State the blood parasite species.
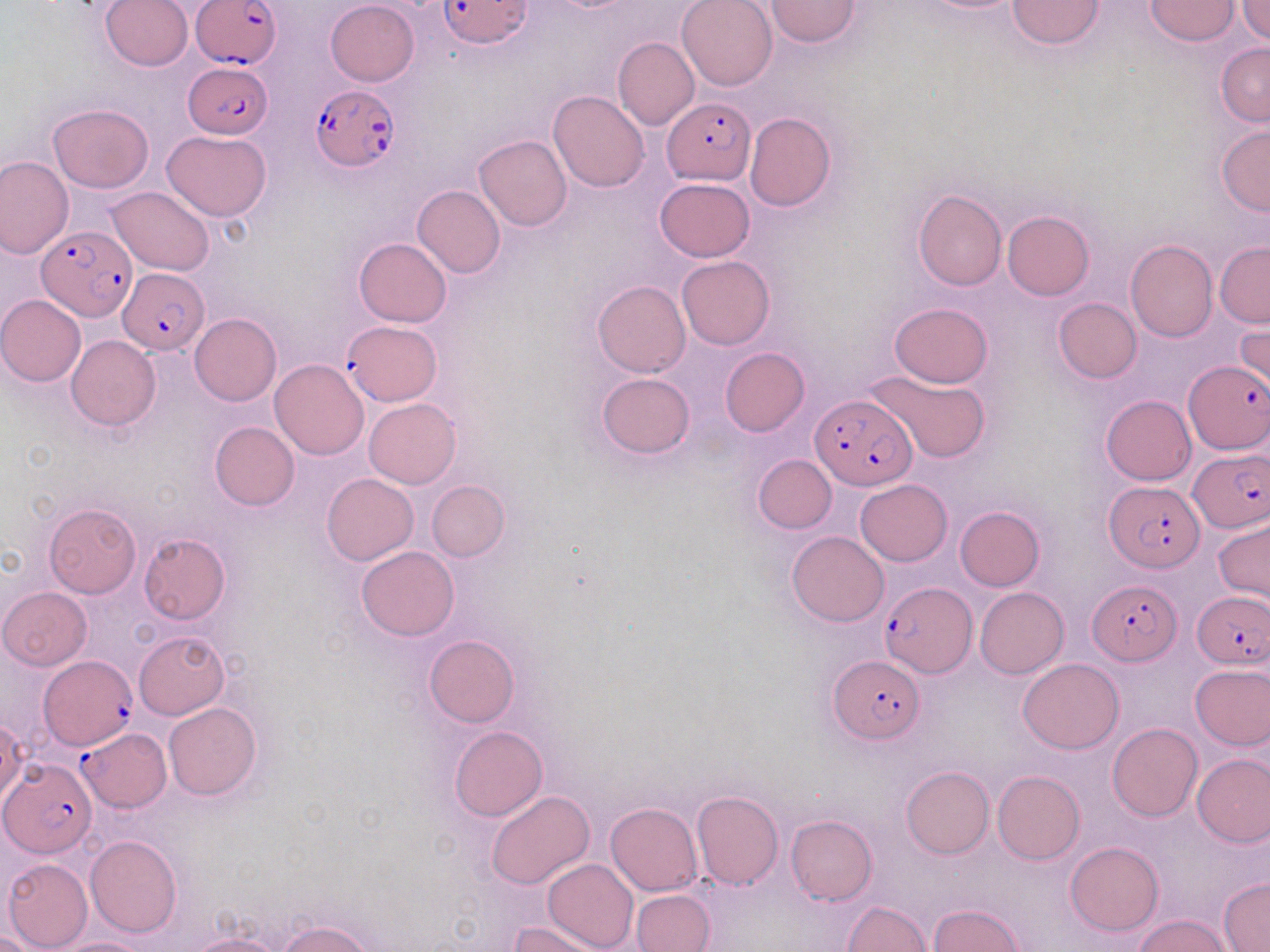
Plasmodium falciparum.

Approximate bounding boxes as named x1/y1/x2/y2 corners in pixels. Plasmodium falciparum-infected red blood cell locations: (x1=190, y1=0, x2=282, y2=68), (x1=437, y1=0, x2=533, y2=49), (x1=187, y1=63, x2=271, y2=140), (x1=310, y1=85, x2=398, y2=172), (x1=662, y1=96, x2=754, y2=183), (x1=36, y1=224, x2=135, y2=323), (x1=118, y1=268, x2=211, y2=355), (x1=342, y1=321, x2=442, y2=405), (x1=1185, y1=360, x2=1270, y2=453), (x1=811, y1=393, x2=915, y2=490), (x1=1190, y1=450, x2=1269, y2=531), (x1=1104, y1=480, x2=1204, y2=571), (x1=1087, y1=580, x2=1180, y2=664), (x1=879, y1=581, x2=974, y2=676), (x1=1193, y1=591, x2=1270, y2=669), (x1=827, y1=654, x2=923, y2=743), (x1=36, y1=655, x2=136, y2=753), (x1=77, y1=727, x2=172, y2=811), (x1=1, y1=759, x2=96, y2=857). Uninfected red blood cell locations: (x1=102, y1=0, x2=192, y2=72), (x1=676, y1=0, x2=777, y2=90), (x1=766, y1=0, x2=861, y2=46), (x1=1008, y1=0, x2=1105, y2=49), (x1=1146, y1=0, x2=1239, y2=44), (x1=1236, y1=0, x2=1270, y2=44), (x1=325, y1=1, x2=419, y2=86), (x1=613, y1=37, x2=698, y2=131), (x1=1217, y1=42, x2=1269, y2=127), (x1=549, y1=89, x2=649, y2=192), (x1=48, y1=104, x2=154, y2=193), (x1=745, y1=112, x2=836, y2=212), (x1=1217, y1=125, x2=1270, y2=217), (x1=161, y1=130, x2=271, y2=221), (x1=474, y1=135, x2=572, y2=231), (x1=0, y1=155, x2=73, y2=258), (x1=654, y1=178, x2=755, y2=261), (x1=412, y1=185, x2=505, y2=278), (x1=106, y1=186, x2=215, y2=275), (x1=912, y1=189, x2=1006, y2=291), (x1=1002, y1=210, x2=1093, y2=300), (x1=353, y1=237, x2=450, y2=327), (x1=1124, y1=239, x2=1217, y2=341), (x1=1214, y1=242, x2=1270, y2=327), (x1=676, y1=256, x2=774, y2=350), (x1=592, y1=280, x2=690, y2=378), (x1=0, y1=295, x2=86, y2=386), (x1=1053, y1=298, x2=1142, y2=383), (x1=888, y1=302, x2=994, y2=387), (x1=189, y1=313, x2=281, y2=406), (x1=1234, y1=325, x2=1269, y2=404), (x1=67, y1=335, x2=161, y2=430), (x1=720, y1=348, x2=809, y2=436), (x1=269, y1=359, x2=369, y2=460), (x1=865, y1=369, x2=991, y2=462), (x1=596, y1=372, x2=696, y2=460), (x1=1101, y1=395, x2=1196, y2=485), (x1=364, y1=399, x2=459, y2=487), (x1=210, y1=421, x2=300, y2=510), (x1=752, y1=454, x2=837, y2=533), (x1=321, y1=473, x2=419, y2=565), (x1=855, y1=479, x2=952, y2=566), (x1=426, y1=480, x2=509, y2=561), (x1=44, y1=503, x2=140, y2=598), (x1=955, y1=506, x2=1044, y2=591), (x1=1214, y1=517, x2=1270, y2=603), (x1=786, y1=530, x2=888, y2=626), (x1=139, y1=533, x2=230, y2=623), (x1=357, y1=546, x2=459, y2=641), (x1=974, y1=586, x2=1068, y2=678), (x1=0, y1=587, x2=91, y2=670), (x1=134, y1=630, x2=230, y2=719), (x1=424, y1=634, x2=520, y2=727), (x1=1018, y1=657, x2=1124, y2=754), (x1=1190, y1=662, x2=1270, y2=750), (x1=164, y1=702, x2=261, y2=800), (x1=1, y1=718, x2=27, y2=806), (x1=1107, y1=723, x2=1202, y2=821), (x1=449, y1=726, x2=548, y2=821), (x1=1193, y1=752, x2=1270, y2=847), (x1=902, y1=766, x2=994, y2=859), (x1=992, y1=771, x2=1085, y2=864), (x1=691, y1=790, x2=782, y2=890), (x1=486, y1=791, x2=594, y2=889), (x1=606, y1=803, x2=702, y2=895), (x1=787, y1=815, x2=877, y2=906), (x1=85, y1=834, x2=181, y2=937), (x1=1066, y1=841, x2=1163, y2=935), (x1=543, y1=857, x2=638, y2=952), (x1=3, y1=859, x2=93, y2=950), (x1=1218, y1=878, x2=1269, y2=951), (x1=631, y1=889, x2=714, y2=951), (x1=841, y1=901, x2=932, y2=952), (x1=930, y1=904, x2=1026, y2=952), (x1=1134, y1=913, x2=1233, y2=952), (x1=279, y1=919, x2=375, y2=952), (x1=510, y1=920, x2=606, y2=952), (x1=184, y1=933, x2=284, y2=952), (x1=53, y1=937, x2=152, y2=952). Single field of view. Thin blood smear. 1000x magnification. Image is 1270×952 pixels. Light microscopy. May-Grünwald-Giemsa stain.